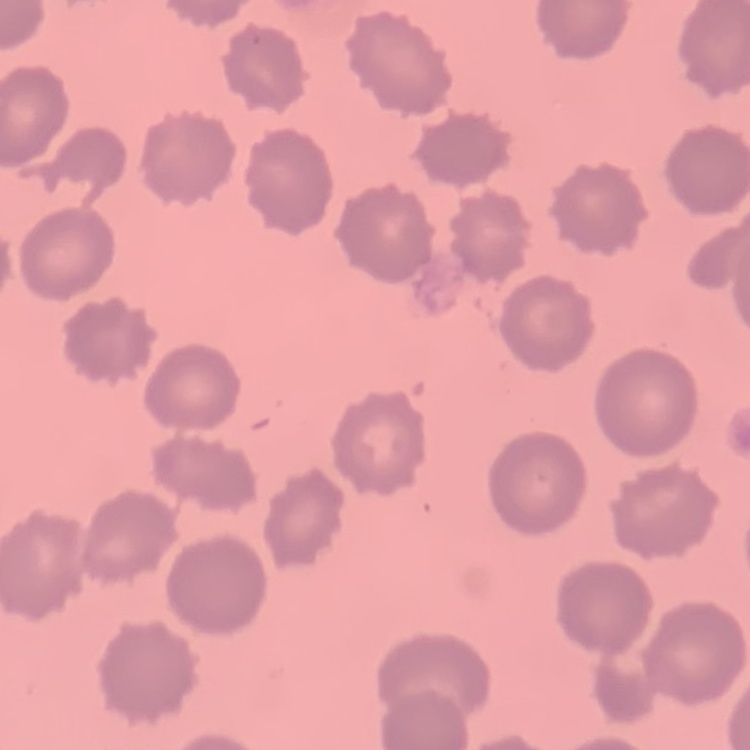

The erythrocytes exhibit no rouleaux formation. Thin peripheral smear. Field's or Giemsa stain. One tile cut from a larger photomicrograph.